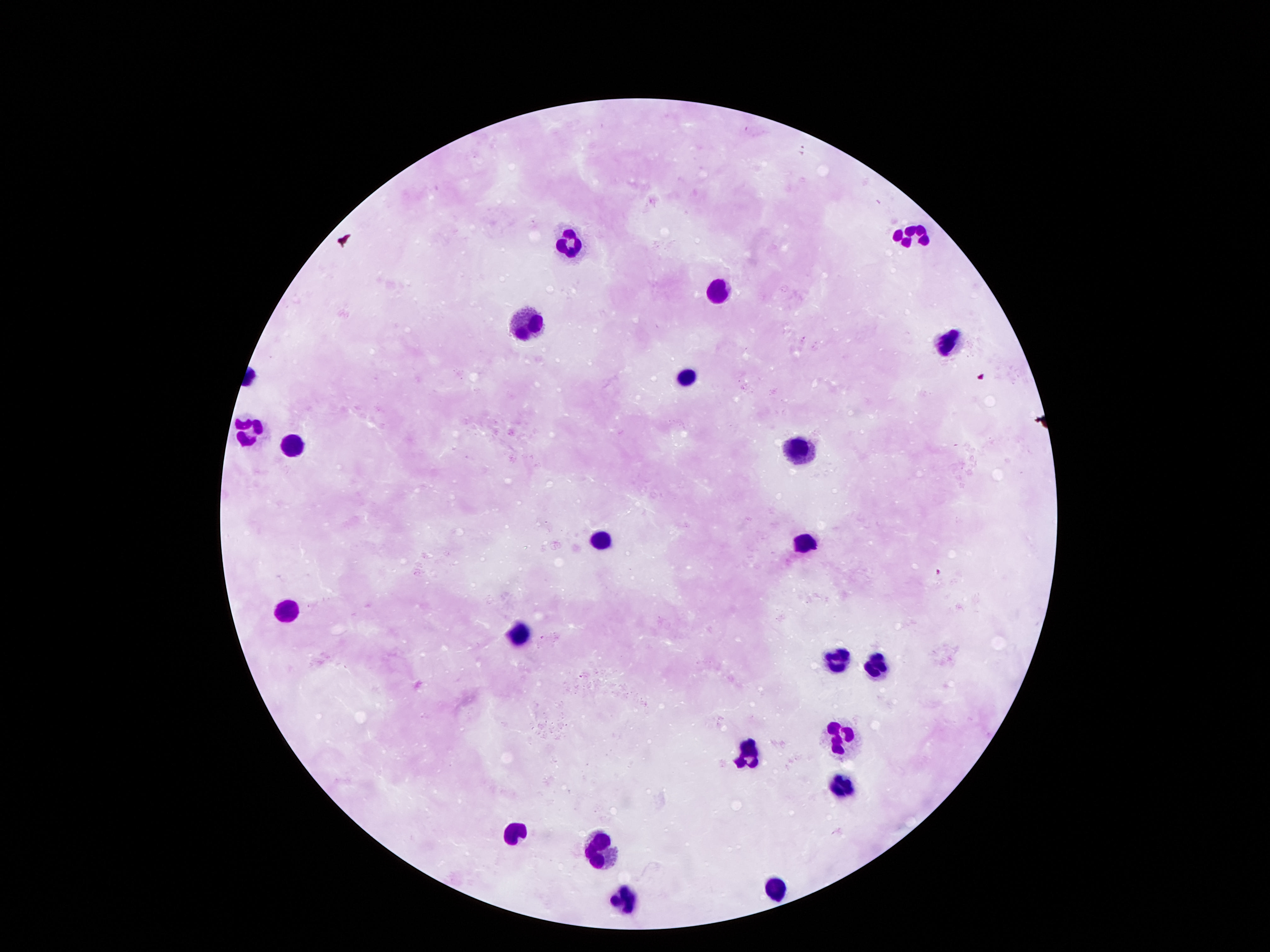 Approximate object centers, in pixels from the top-left corner. Leukocyte locations: (x=913, y=234), (x=571, y=237), (x=723, y=290), (x=524, y=321), (x=947, y=338), (x=690, y=378), (x=256, y=427), (x=294, y=444), (x=800, y=447), (x=604, y=540), (x=804, y=540), (x=284, y=610), (x=520, y=631), (x=843, y=653), (x=879, y=664), (x=843, y=737), (x=751, y=749), (x=843, y=780), (x=515, y=832), (x=603, y=849), (x=774, y=884), (x=625, y=899). Smartphone photograph taken through the microscope eyepiece. Image is 1270×952 pixels. One field from this slide. Thick peripheral-blood smear. 100x magnification. Giemsa-stained preparation. Patient malaria status: not infected.